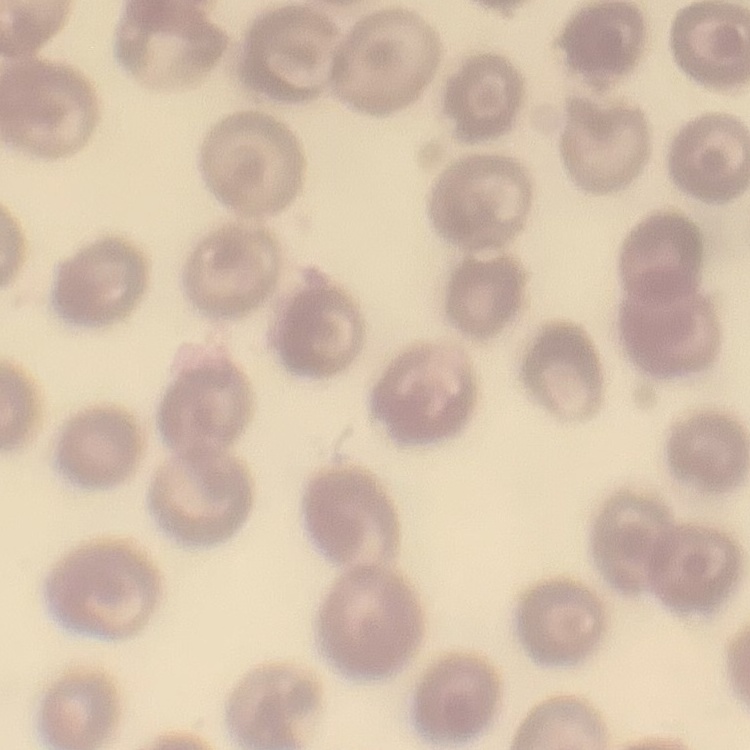
erythrocyte morphology = no rouleaux formation
stain = Field's or Giemsa
image type = square crop of a larger photomicrograph
preparation = thin peripheral smear